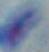

modality = micrograph
identification = Toxoplasma gondii
magnification = 1000x